Locate every uninfected red blood cell.
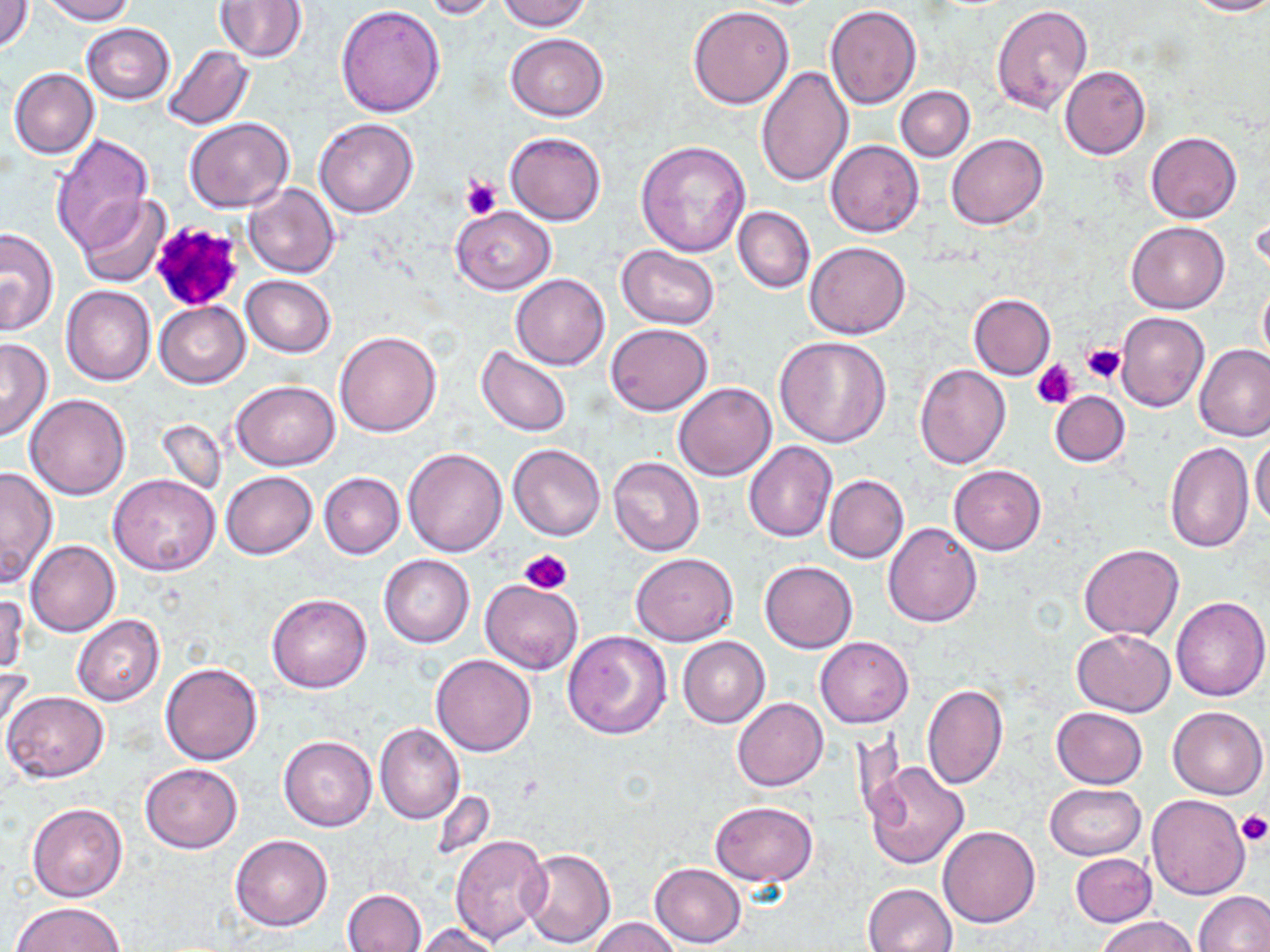

Approximate bounding boxes as named x1/y1/x2/y2 corners in pixels.
Uninfected red blood cells: (x1=2, y1=0, x2=33, y2=52), (x1=39, y1=0, x2=137, y2=24), (x1=421, y1=0, x2=500, y2=21), (x1=497, y1=0, x2=593, y2=32), (x1=1186, y1=0, x2=1270, y2=17), (x1=215, y1=2, x2=307, y2=62), (x1=991, y1=3, x2=1094, y2=115), (x1=335, y1=4, x2=445, y2=116), (x1=824, y1=5, x2=922, y2=110), (x1=686, y1=6, x2=794, y2=110), (x1=82, y1=22, x2=175, y2=103), (x1=505, y1=32, x2=608, y2=120), (x1=160, y1=43, x2=254, y2=131), (x1=754, y1=65, x2=852, y2=187), (x1=1060, y1=65, x2=1151, y2=160), (x1=9, y1=68, x2=99, y2=160), (x1=895, y1=86, x2=974, y2=161), (x1=185, y1=118, x2=295, y2=212), (x1=314, y1=118, x2=421, y2=218), (x1=1145, y1=130, x2=1241, y2=224), (x1=505, y1=131, x2=606, y2=226), (x1=946, y1=133, x2=1047, y2=230), (x1=52, y1=134, x2=155, y2=253), (x1=825, y1=139, x2=924, y2=238), (x1=635, y1=140, x2=751, y2=257), (x1=243, y1=183, x2=340, y2=278), (x1=77, y1=194, x2=170, y2=288), (x1=450, y1=206, x2=556, y2=294), (x1=733, y1=206, x2=815, y2=293), (x1=1127, y1=220, x2=1229, y2=313), (x1=0, y1=227, x2=59, y2=335), (x1=805, y1=241, x2=910, y2=339), (x1=616, y1=245, x2=720, y2=329), (x1=242, y1=274, x2=337, y2=357), (x1=511, y1=274, x2=610, y2=370), (x1=1257, y1=281, x2=1270, y2=370), (x1=60, y1=286, x2=156, y2=386), (x1=968, y1=293, x2=1055, y2=380), (x1=154, y1=301, x2=250, y2=388), (x1=1116, y1=311, x2=1209, y2=412), (x1=607, y1=324, x2=713, y2=415), (x1=335, y1=331, x2=441, y2=438), (x1=774, y1=335, x2=892, y2=448), (x1=0, y1=337, x2=52, y2=444), (x1=1194, y1=343, x2=1270, y2=442), (x1=475, y1=346, x2=574, y2=437), (x1=914, y1=365, x2=1011, y2=470), (x1=231, y1=380, x2=340, y2=470), (x1=673, y1=382, x2=777, y2=481), (x1=1049, y1=390, x2=1130, y2=467), (x1=24, y1=393, x2=133, y2=500), (x1=156, y1=418, x2=227, y2=498), (x1=1251, y1=435, x2=1270, y2=528), (x1=1165, y1=440, x2=1255, y2=554), (x1=743, y1=441, x2=837, y2=543), (x1=508, y1=443, x2=605, y2=541), (x1=401, y1=447, x2=507, y2=557), (x1=607, y1=456, x2=704, y2=556), (x1=949, y1=464, x2=1046, y2=555), (x1=0, y1=465, x2=58, y2=587), (x1=220, y1=470, x2=318, y2=559), (x1=319, y1=472, x2=404, y2=559), (x1=108, y1=474, x2=221, y2=577), (x1=823, y1=474, x2=908, y2=563), (x1=882, y1=522, x2=982, y2=628), (x1=25, y1=540, x2=119, y2=637), (x1=1078, y1=543, x2=1185, y2=641), (x1=630, y1=552, x2=739, y2=646), (x1=378, y1=555, x2=475, y2=648), (x1=760, y1=560, x2=857, y2=653), (x1=479, y1=579, x2=583, y2=675), (x1=1, y1=591, x2=28, y2=679), (x1=266, y1=593, x2=372, y2=693), (x1=1171, y1=595, x2=1270, y2=701), (x1=72, y1=615, x2=165, y2=707), (x1=1071, y1=629, x2=1176, y2=716), (x1=563, y1=630, x2=672, y2=739), (x1=678, y1=636, x2=770, y2=728), (x1=814, y1=636, x2=914, y2=728), (x1=431, y1=654, x2=537, y2=756), (x1=0, y1=656, x2=36, y2=747), (x1=160, y1=661, x2=263, y2=765), (x1=922, y1=683, x2=1007, y2=789), (x1=2, y1=690, x2=109, y2=783), (x1=733, y1=697, x2=828, y2=792), (x1=1168, y1=705, x2=1267, y2=800), (x1=1050, y1=707, x2=1147, y2=789), (x1=375, y1=723, x2=463, y2=824), (x1=278, y1=735, x2=377, y2=831), (x1=863, y1=761, x2=969, y2=869), (x1=141, y1=762, x2=242, y2=852), (x1=1045, y1=783, x2=1146, y2=861), (x1=1146, y1=794, x2=1251, y2=900), (x1=711, y1=801, x2=817, y2=887), (x1=26, y1=803, x2=128, y2=902), (x1=938, y1=826, x2=1039, y2=928), (x1=450, y1=834, x2=552, y2=946), (x1=230, y1=835, x2=332, y2=932), (x1=520, y1=847, x2=615, y2=948), (x1=1070, y1=853, x2=1156, y2=927), (x1=649, y1=862, x2=745, y2=947), (x1=862, y1=882, x2=957, y2=952), (x1=342, y1=889, x2=426, y2=951), (x1=1194, y1=891, x2=1270, y2=952), (x1=11, y1=903, x2=125, y2=952), (x1=588, y1=916, x2=680, y2=952), (x1=1095, y1=916, x2=1200, y2=952), (x1=412, y1=923, x2=504, y2=952).

slide-level diagnosis = negative for blood parasites
preparation = thin blood smear
magnification = 1000x
image size = 1270×952 pixels
field of view = single
stain = May-Grünwald-Giemsa
modality = light microscopy
platelet locations = approximate bounding boxes as named x1/y1/x2/y2 corners in pixels: (x1=459, y1=173, x2=502, y2=221), (x1=150, y1=223, x2=248, y2=315), (x1=1081, y1=343, x2=1127, y2=384), (x1=1031, y1=359, x2=1079, y2=409), (x1=519, y1=548, x2=572, y2=596), (x1=1234, y1=810, x2=1270, y2=847)